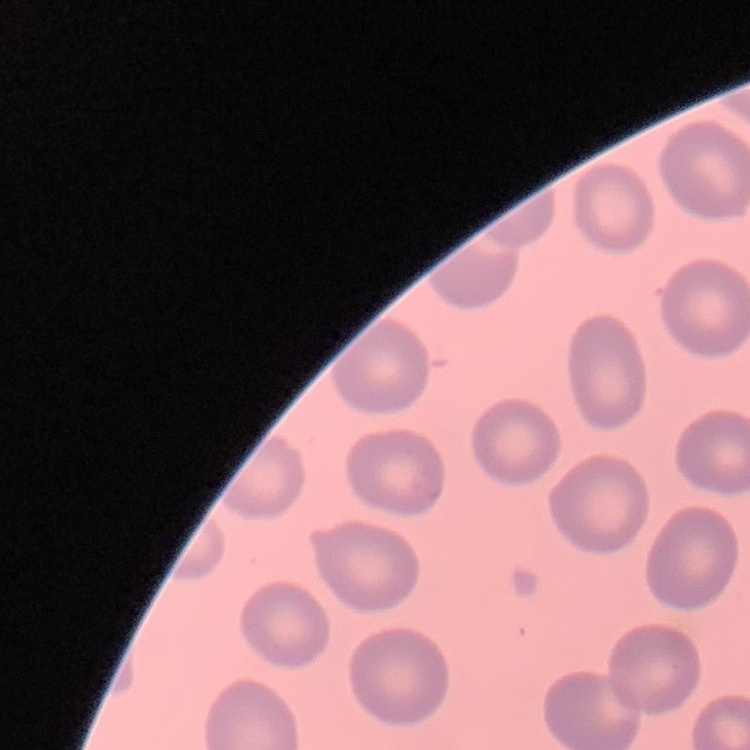
red blood cell morphology = no rouleaux formation
preparation = thin peripheral smear
image type = square crop of a larger photomicrograph
stain = Field's or Giemsa